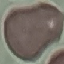 Result: no malaria parasites seen. Automatically extracted cell patch, resized to 64 × 64 pixels. Acquired by smartphone through the microscope eyepiece. Giemsa-stained preparation. Thin blood smear.